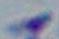

Summary:
  - Identification: Toxoplasma gondii
  - Modality: micrograph
  - Magnification: 1000x